Point out each Plasmodium parasite.
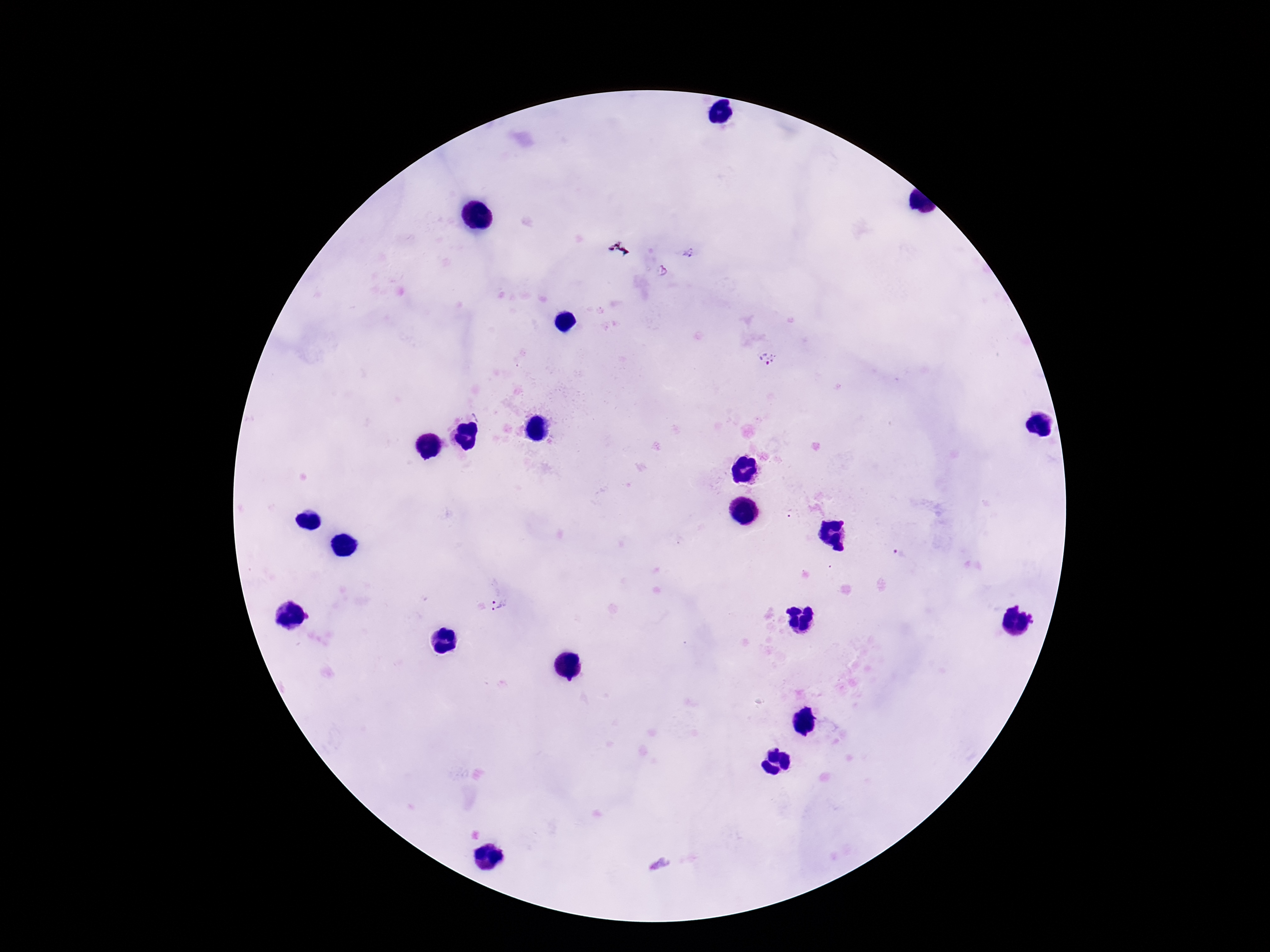
Approximate centers as {x, y} in pixels.
Plasmodium parasites: {689, 252}, {767, 358}, {899, 553}, {501, 604}.

Summary:
  - Capture: smartphone camera through the microscope eyepiece
  - Preparation: thick peripheral-blood smear
  - Magnification: 100x
  - Field of view: single
  - Image size: 1270×952 pixels
  - Stain: Giemsa
  - Patient malaria status: infected